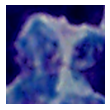
{
  "modality": "photomicrograph",
  "magnification": "1000x",
  "identification": "white blood cell"
}